Assess for malaria.
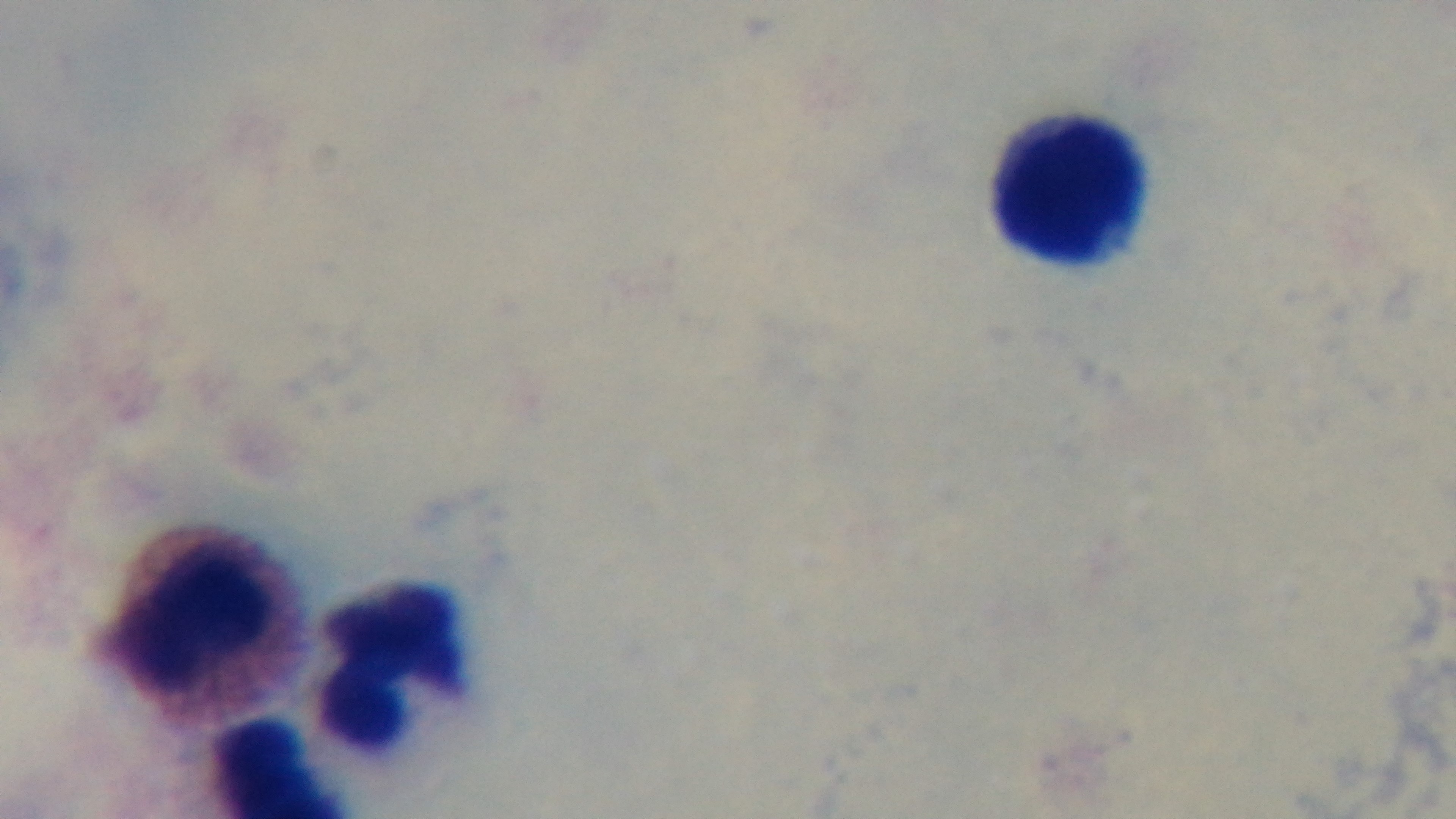
Negative.

Summary:
  - Objective: 100x oil immersion
  - Preparation: thick smear
  - Stain: Giemsa
  - Capture: mounted 4K digital camera
  - Field of view: single
  - Modality: light microscopy